Describe the morphology of the red blood cells.
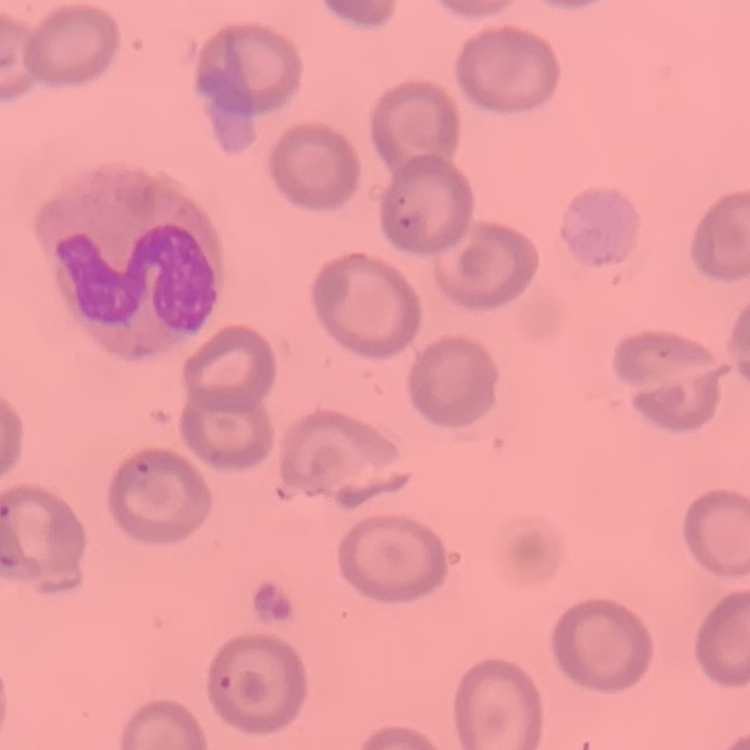

No rouleaux formation.

image type = one tile cut from a larger photomicrograph
preparation = thin blood film
stain = Field's or Giemsa